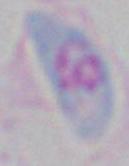

Summary:
  - Modality: micrograph
  - Identification: Toxoplasma gondii
  - Magnification: 1000x